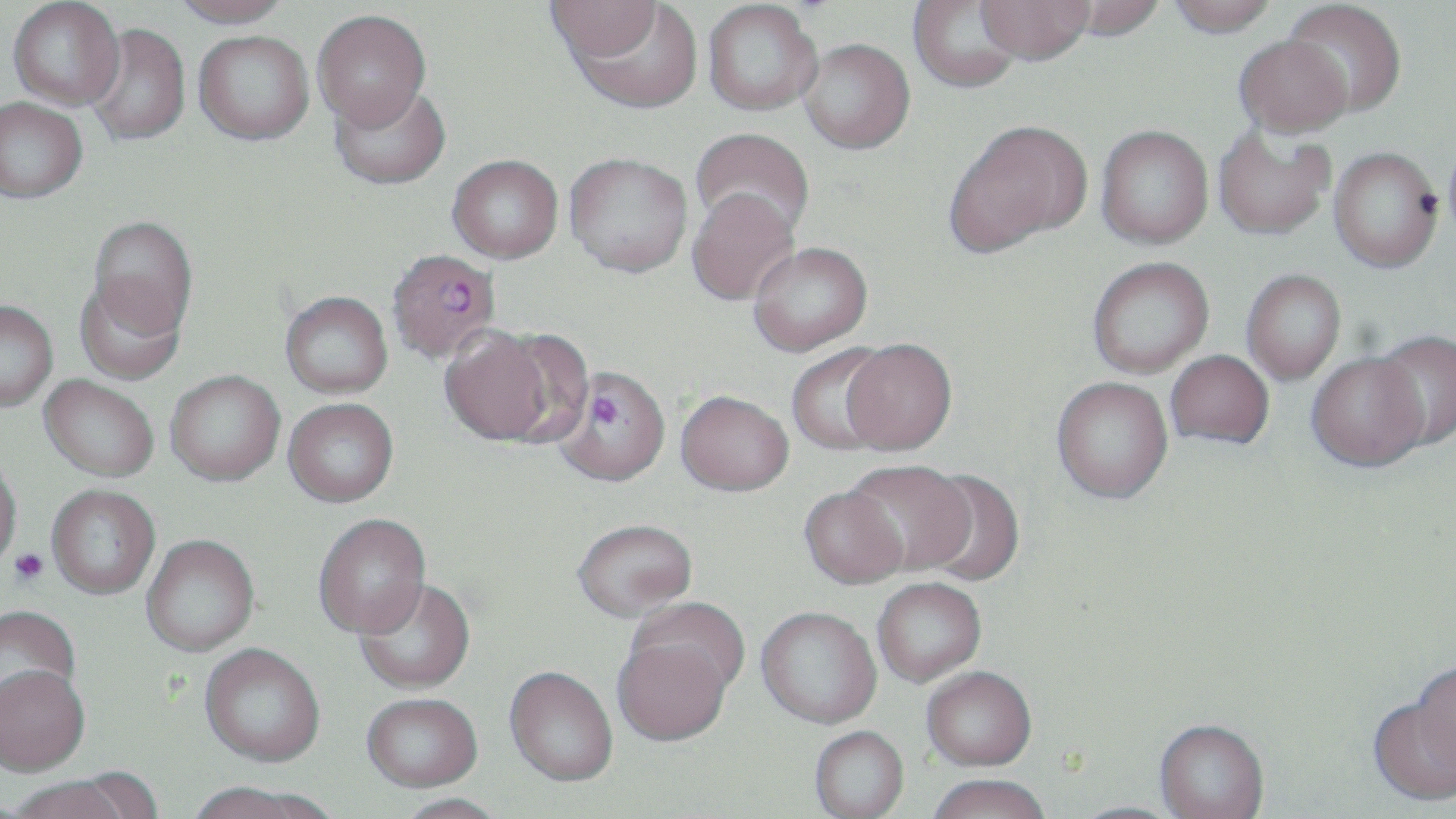
Approximate bounding boxes as (x1, y1, x2, y2) in pixels. Uninfected red blood cell locations: (170, 0, 294, 28), (908, 0, 1024, 93), (975, 0, 1094, 65), (1056, 0, 1169, 42), (1166, 0, 1280, 37), (1284, 0, 1407, 117), (8, 1, 124, 110), (545, 1, 662, 62), (702, 1, 822, 115), (567, 2, 704, 114), (312, 10, 431, 130), (84, 24, 190, 146), (193, 30, 314, 145), (1233, 34, 1354, 138), (797, 38, 914, 154), (328, 79, 451, 191), (0, 97, 87, 203), (945, 118, 1090, 255), (1096, 125, 1213, 248), (1213, 125, 1335, 241), (690, 128, 814, 241), (1329, 147, 1443, 272), (564, 152, 693, 277), (447, 155, 563, 263), (687, 187, 800, 306), (87, 215, 198, 341), (747, 241, 873, 356), (1087, 257, 1214, 378), (1242, 269, 1346, 384), (75, 274, 186, 384), (280, 290, 392, 398), (0, 300, 58, 411), (439, 327, 562, 447), (1373, 330, 1456, 452), (840, 340, 957, 457), (785, 345, 895, 456), (1166, 351, 1274, 450), (1306, 353, 1429, 472), (165, 370, 285, 486), (39, 375, 159, 481), (1051, 379, 1174, 507), (675, 392, 794, 500), (282, 398, 399, 508), (0, 451, 23, 570), (844, 463, 975, 579), (918, 471, 1024, 588), (46, 485, 161, 599), (798, 489, 908, 593), (313, 514, 432, 641), (572, 523, 698, 625), (141, 535, 259, 658), (354, 580, 477, 696), (873, 580, 986, 689), (626, 598, 750, 704), (0, 607, 83, 720), (756, 609, 882, 731), (613, 631, 735, 751), (199, 647, 325, 771), (1411, 664, 1456, 781), (0, 669, 90, 780), (504, 670, 618, 789), (921, 670, 1037, 775), (361, 697, 483, 796), (1367, 698, 1456, 807), (1154, 722, 1269, 819), (809, 728, 910, 819), (68, 767, 166, 819), (926, 778, 1050, 819), (7, 780, 133, 819), (184, 785, 329, 819), (395, 797, 508, 819), (1067, 802, 1186, 819). Plasmodium falciparum-infected red blood cell locations: (386, 248, 501, 363), (554, 369, 671, 491). Platelet locations: (9, 548, 49, 585). Slide-level diagnosis: Plasmodium falciparum. Thin blood film. Image is 1456×819 pixels. Light microscopy. One field of a larger specimen. May-Grünwald-Giemsa stain. Captured at 1000x magnification.